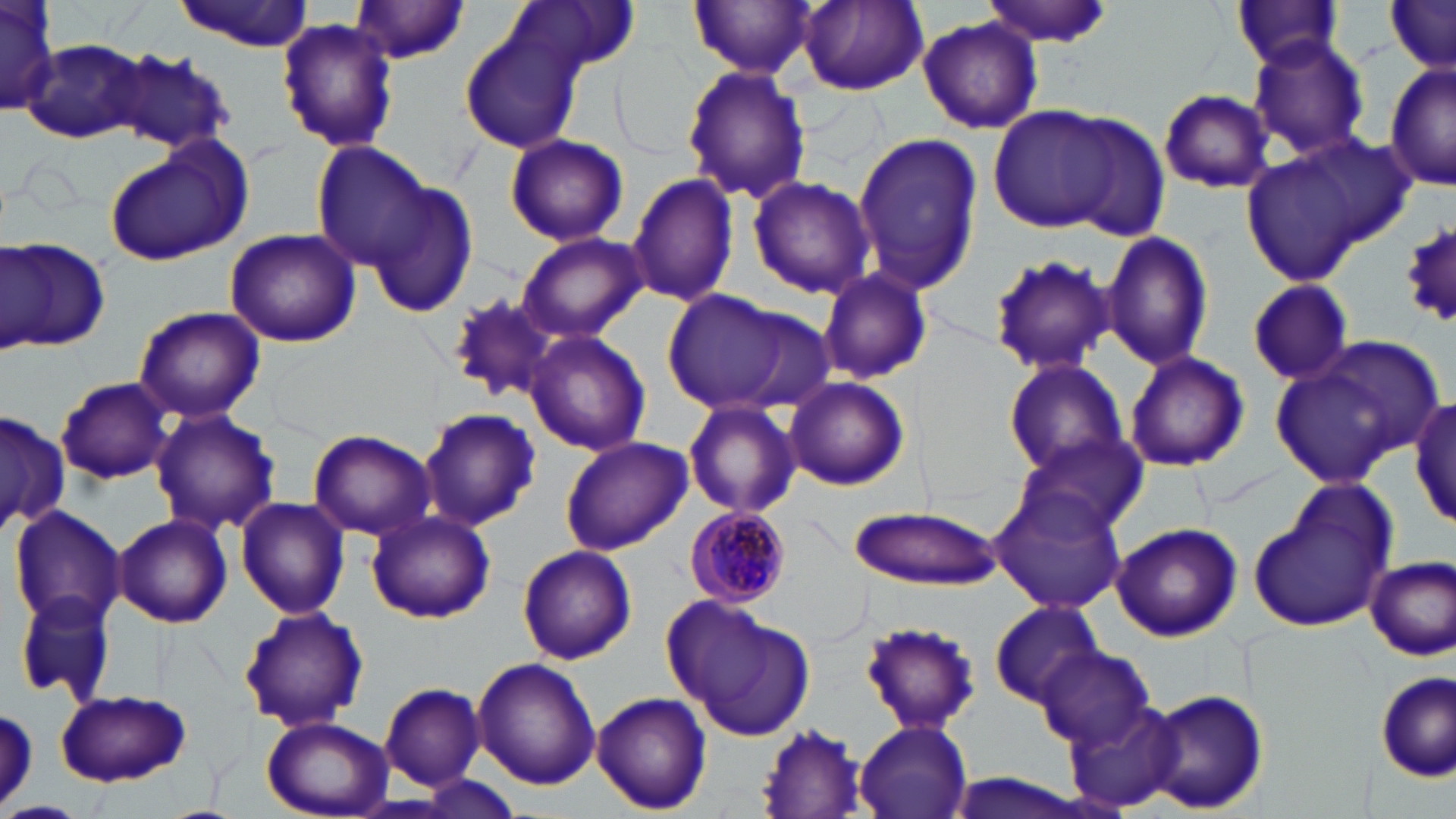
{
  "slide_level_diagnosis": "Plasmodium malariae",
  "stain": "May-Grünwald-Giemsa",
  "magnification": "1000x",
  "plasmodium_malariae_infected_red_blood_cell_locations": "approximate bounding boxes as (x1, y1, x2, y2) in pixels: (684, 507, 793, 610)",
  "image_size": "1456×819 pixels",
  "modality": "optical microscopy",
  "preparation": "thin blood smear",
  "uninfected_red_blood_cell_locations": "approximate bounding boxes as (x1, y1, x2, y2) in pixels: (0, 0, 58, 111), (688, 0, 816, 78), (797, 0, 927, 95), (980, 0, 1114, 48), (1229, 0, 1348, 71), (173, 1, 315, 50), (510, 1, 642, 76), (1386, 1, 1456, 71), (347, 2, 474, 63), (916, 15, 1045, 136), (275, 17, 400, 153), (460, 23, 584, 154), (1246, 33, 1372, 161), (23, 38, 153, 144), (109, 50, 237, 154), (1384, 61, 1454, 193), (681, 64, 811, 205), (1157, 88, 1275, 193), (987, 104, 1134, 233), (850, 132, 984, 297), (504, 135, 627, 247), (1241, 138, 1407, 287), (102, 139, 248, 265), (313, 141, 438, 269), (626, 171, 740, 308), (747, 176, 878, 300), (367, 182, 478, 319), (1402, 225, 1456, 327), (224, 228, 362, 349), (516, 231, 646, 343), (1100, 231, 1214, 371), (2, 240, 112, 354), (987, 252, 1115, 377), (820, 266, 934, 384), (1244, 280, 1356, 383), (662, 288, 819, 418), (445, 294, 561, 406), (133, 305, 266, 425), (525, 332, 652, 456), (1274, 337, 1440, 483), (1124, 350, 1250, 471), (999, 359, 1132, 479), (56, 376, 174, 485), (784, 377, 910, 492), (1411, 394, 1456, 530), (682, 399, 802, 520), (419, 407, 540, 532), (150, 409, 281, 535), (0, 410, 70, 535), (306, 429, 436, 541), (560, 434, 693, 555), (1010, 435, 1146, 539), (1249, 481, 1395, 633), (988, 486, 1130, 616), (235, 496, 351, 619), (847, 505, 1002, 591), (8, 506, 125, 629), (364, 508, 497, 624), (113, 512, 234, 629), (1112, 522, 1242, 642), (516, 544, 637, 665), (1364, 555, 1456, 660), (13, 589, 118, 704), (675, 599, 817, 742), (989, 600, 1104, 709), (237, 605, 369, 732), (857, 620, 984, 734), (1035, 646, 1153, 748), (472, 659, 599, 790), (1375, 672, 1454, 782), (380, 683, 484, 790), (1145, 687, 1267, 814), (53, 690, 193, 787), (590, 691, 712, 814), (1062, 696, 1186, 811), (0, 703, 38, 808), (260, 715, 393, 817), (754, 720, 869, 819), (853, 720, 974, 818), (0, 799, 83, 819)",
  "field_of_view": "one of a larger specimen"
}